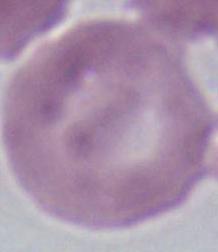
magnification = 1000x
identification = erythrocyte
modality = photomicrograph